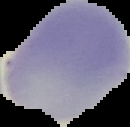
Summary:
  - Malaria status: uninfected
  - Image type: segmented cell region with the area outside set to black
  - Preparation: thin blood film
  - Image size: 130×127 pixels